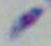
Summary:
  - Modality: micrograph
  - Identification: Toxoplasma gondii
  - Magnification: 1000x